State which parasite is depicted.
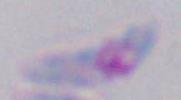
This is Toxoplasma gondii.

Captured at 1000x magnification. Photomicrograph.